Identify the preparation type.
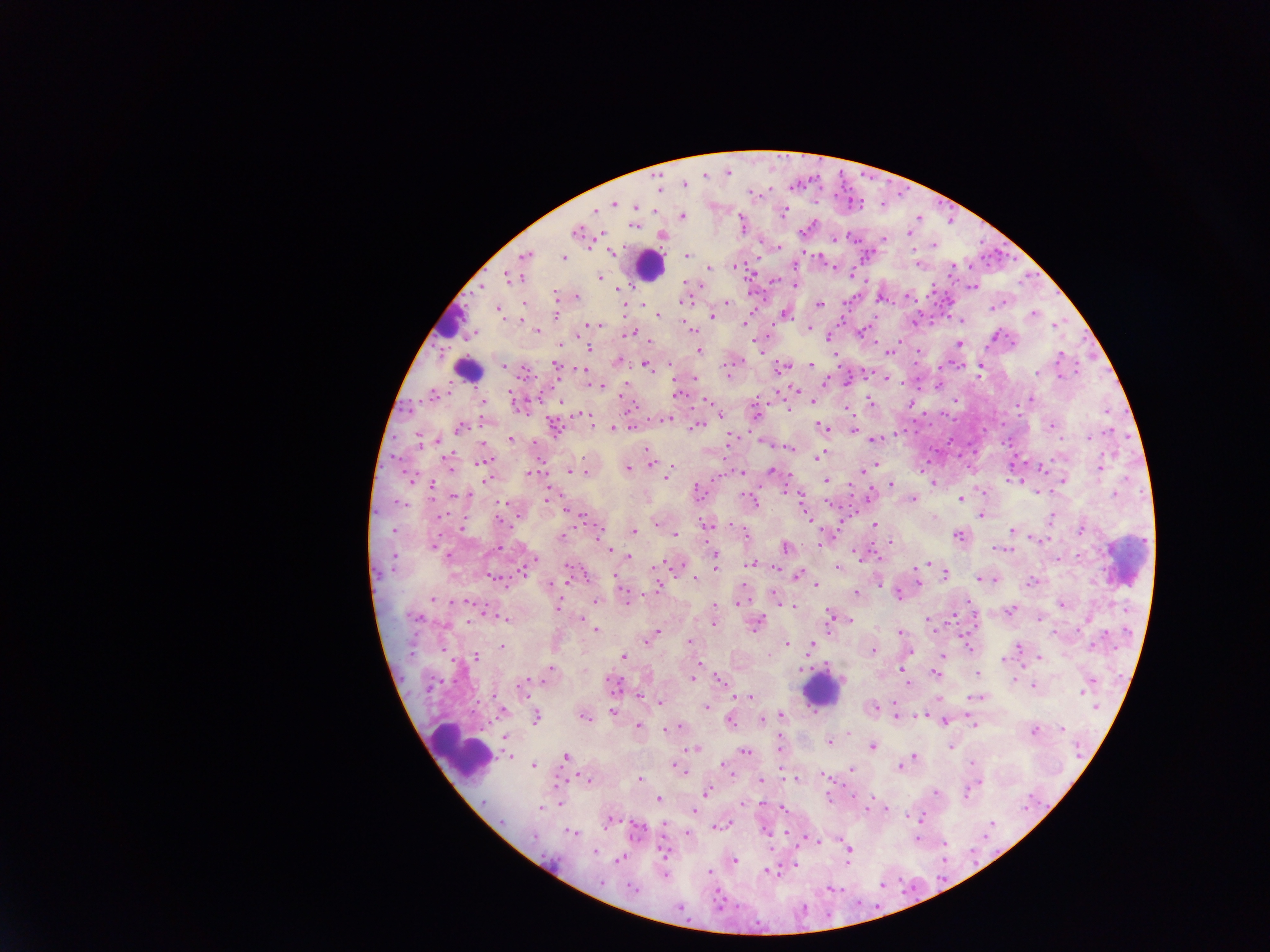

Thick blood smear.

leukocyte_locations: 'approximate centers as {x, y} in pixels (subset; some below the resolvable size): {649, 267}, {451, 323}, {468, 368}, {1124, 563}, {822, 691}, {460, 754}'
capture: mobile-phone photograph through a microscope
field_of_view: single
country: Ghana
image_size: 1270×952 pixels
malaria_parasite_locations: 'approximate centers as {x, y} in pixels: {729, 172}, {705, 176}, {685, 184}, {800, 184}, {660, 188}, {770, 189}, {753, 194}, {614, 204}, {854, 204}, {883, 205}, {637, 207}, {655, 210}, {596, 212}, {785, 213}, {683, 217}, {919, 217}, {743, 225}, {636, 226}, {580, 232}, {910, 234}, {663, 237}, {836, 239}, {853, 239}, {884, 239}, {935, 245}, {613, 253}, {687, 256}, {565, 260}, {919, 265}, {710, 269}, {600, 278}, {795, 285}, {975, 287}, {618, 290}, {556, 295}, {576, 297}, {525, 304}, {820, 304}, {727, 305}, {642, 306}, {994, 308}, {501, 314}, {659, 316}, {557, 317}, {712, 318}, {745, 324}, {598, 326}, {810, 329}, {538, 331}, {633, 333}, {830, 341}, {649, 342}, {960, 343}, {560, 345}, {591, 349}, {700, 351}, {890, 353}, {619, 361}, {812, 365}, {647, 366}, {503, 367}, {557, 367}, {781, 369}, {981, 370}, {729, 374}, {593, 386}, {678, 395}, {484, 402}, {813, 402}, {872, 403}, {912, 406}, {789, 410}, {757, 414}, {581, 415}, {721, 415}, {696, 428}, {823, 428}, {460, 429}, {612, 429}, {855, 429}, {511, 440}, {733, 440}, {875, 441}, {484, 443}, {791, 448}, {820, 458}, {652, 463}, {875, 466}, {1101, 469}, {629, 470}, {771, 471}, {863, 471}, {586, 472}, {570, 473}, {742, 473}, {530, 474}, {668, 476}, {487, 479}, {827, 481}, {1064, 482}, {934, 484}, {892, 485}, {786, 492}, {698, 494}, {1037, 494}, {1116, 495}, {799, 497}, {914, 500}, {962, 500}, {755, 503}, {564, 509}, {983, 516}, {808, 517}, {518, 518}, {935, 518}, {1052, 519}, {657, 524}, {708, 525}, {875, 526}, {463, 528}, {1014, 531}, {1082, 531}, {635, 532}, {676, 537}, {959, 537}, {564, 538}, {889, 543}, {786, 548}, {1001, 549}, {610, 550}, {716, 557}, {629, 558}, {716, 565}, {753, 565}, {840, 568}, {798, 575}, {946, 576}, {696, 579}, {919, 579}, {569, 580}, {982, 580}, {996, 581}, {1033, 583}, {879, 585}, {817, 586}, {659, 587}, {857, 594}, {900, 596}, {434, 599}, {468, 602}, {597, 602}, {627, 603}, {740, 604}, {559, 606}, {714, 606}, {1062, 606}, {793, 607}, {1012, 611}, {419, 617}, {832, 617}, {582, 621}, {469, 622}, {714, 624}, {757, 625}, {596, 632}, {901, 632}, {1054, 632}, {658, 634}, {650, 641}, {690, 642}, {787, 645}, {812, 647}, {503, 648}, {969, 648}, {1019, 648}, {442, 651}, {874, 651}, {413, 653}, {911, 653}, {943, 654}, {625, 657}, {477, 659}, {1040, 659}, {1005, 661}, {700, 663}, {552, 669}, {803, 669}, {902, 669}, {978, 673}, {936, 674}, {693, 679}, {719, 679}, {1014, 680}, {528, 681}, {615, 685}, {908, 685}, {524, 687}, {1033, 687}, {432, 688}, {1083, 693}, {640, 697}, {750, 697}, {977, 698}, {660, 704}, {707, 708}, {876, 708}, {1096, 708}, {614, 713}, {896, 715}, {781, 716}, {537, 718}, {586, 718}, {731, 721}, {763, 721}, {945, 723}, {975, 725}, {638, 727}, {680, 727}, {1063, 730}, {664, 731}, {1035, 731}, {849, 735}, {506, 736}, {830, 742}, {781, 746}, {873, 748}, {953, 748}, {696, 749}, {1078, 751}, {745, 753}, {510, 757}, {566, 757}, {914, 759}, {973, 764}, {533, 767}, {675, 767}, {725, 767}, {902, 767}, {680, 770}, {853, 770}, {728, 771}, {824, 775}, {641, 779}, {796, 780}, {762, 781}, {559, 782}, {588, 782}, {708, 793}, {937, 793}, {967, 796}, {658, 799}, {830, 799}, {745, 803}, {1030, 803}, {483, 804}, {561, 804}, {761, 804}, {1026, 807}, {541, 808}, {784, 808}, {868, 809}, {884, 809}, {695, 811}, {921, 818}, {502, 823}, {610, 823}, {992, 825}, {664, 826}, {723, 826}, {638, 831}, {766, 832}, {573, 833}, {990, 833}, {689, 835}, {788, 835}, {769, 836}, {535, 839}, {919, 839}, {817, 842}, {944, 845}, {665, 852}, {596, 853}, {973, 854}, {849, 855}, {621, 859}, {945, 860}, {736, 861}, {796, 864}, {770, 871}, {711, 873}, {779, 873}, {666, 877}, {883, 886}, {833, 890}, {635, 891}, {721, 906}, {682, 910}'